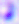 Toxoplasma gondii is shown. 400x magnification. Photomicrograph.